Comment on the morphology of the red blood cells.
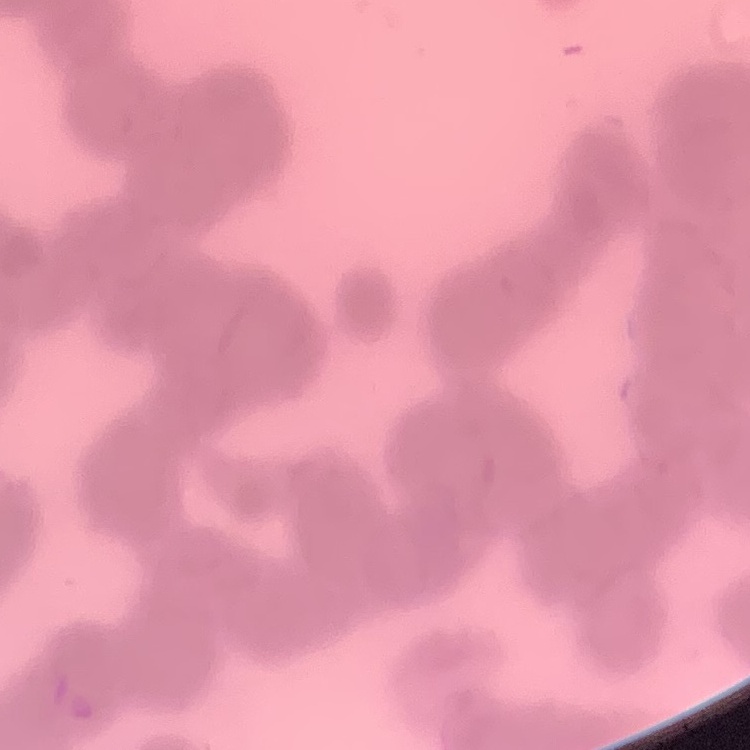
Rouleaux formation.

preparation = thin blood film
image type = square crop of a larger photomicrograph
stain = Field's or Giemsa